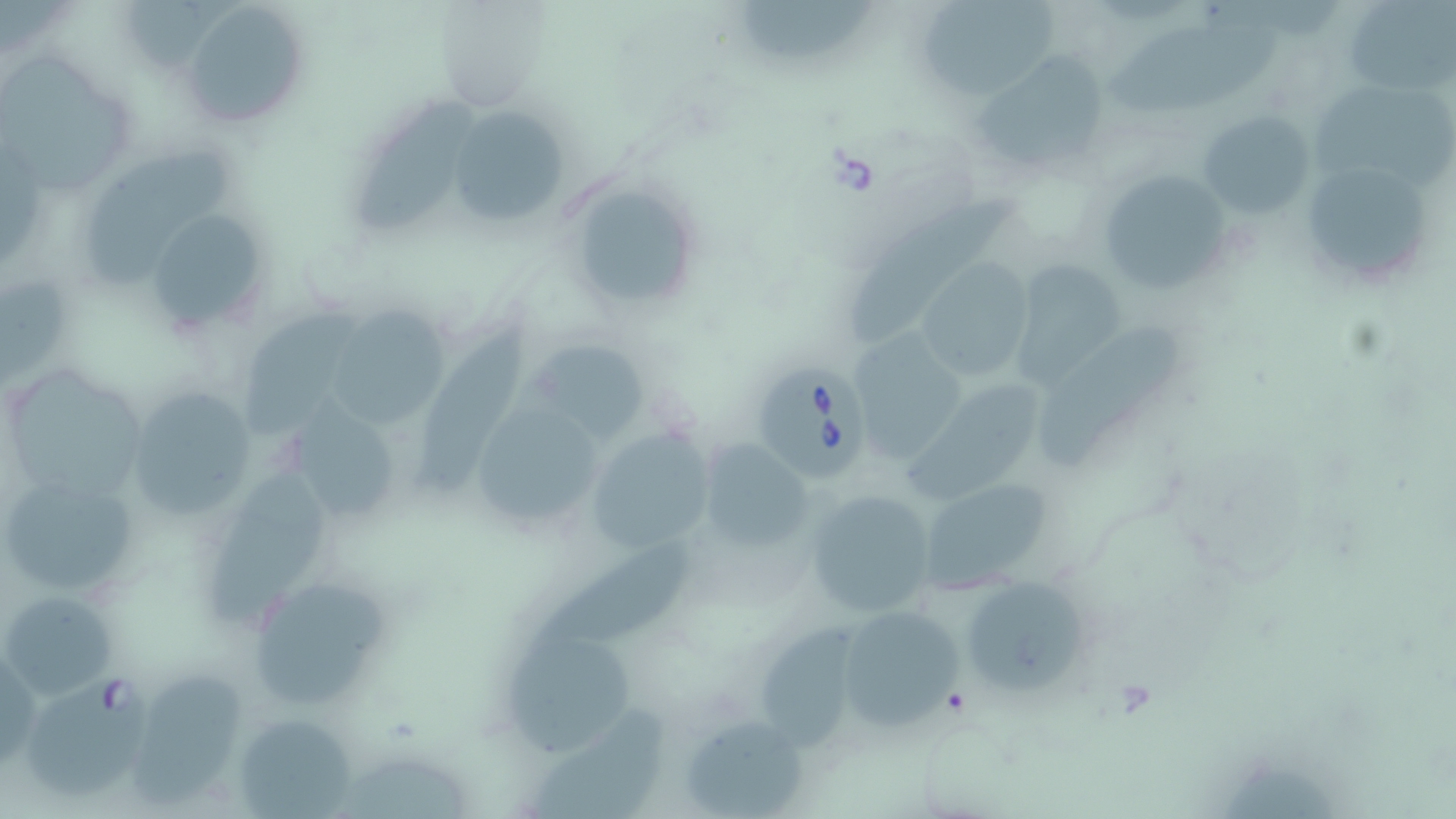
Summary:
  - Coordinate format: approximate bounding boxes as named x1/y1/x2/y2 corners in pixels
  - Uninfected red blood cell locations: (x1=730, y1=0, x2=879, y2=61), (x1=919, y1=0, x2=1058, y2=101), (x1=1343, y1=0, x2=1454, y2=94), (x1=183, y1=1, x2=310, y2=127), (x1=433, y1=3, x2=547, y2=113), (x1=1110, y1=19, x2=1282, y2=110), (x1=975, y1=52, x2=1114, y2=173), (x1=4, y1=54, x2=136, y2=192), (x1=1315, y1=86, x2=1456, y2=188), (x1=354, y1=100, x2=477, y2=240), (x1=445, y1=105, x2=565, y2=227), (x1=1198, y1=109, x2=1316, y2=221), (x1=86, y1=143, x2=225, y2=289), (x1=1299, y1=157, x2=1439, y2=287), (x1=1094, y1=168, x2=1235, y2=296), (x1=566, y1=172, x2=703, y2=312), (x1=847, y1=200, x2=1013, y2=350), (x1=142, y1=207, x2=276, y2=338), (x1=913, y1=258, x2=1032, y2=383), (x1=1007, y1=258, x2=1130, y2=386), (x1=333, y1=301, x2=448, y2=425), (x1=248, y1=307, x2=360, y2=440), (x1=1045, y1=323, x2=1180, y2=464), (x1=416, y1=324, x2=529, y2=499), (x1=855, y1=327, x2=971, y2=467), (x1=527, y1=337, x2=653, y2=442), (x1=3, y1=364, x2=152, y2=507), (x1=914, y1=379, x2=1039, y2=498), (x1=126, y1=385, x2=259, y2=519), (x1=463, y1=395, x2=611, y2=540), (x1=276, y1=403, x2=408, y2=524), (x1=583, y1=429, x2=713, y2=553), (x1=695, y1=440, x2=813, y2=554), (x1=0, y1=472, x2=140, y2=600), (x1=917, y1=476, x2=1061, y2=589), (x1=203, y1=477, x2=328, y2=625), (x1=802, y1=488, x2=938, y2=621), (x1=542, y1=539, x2=697, y2=638), (x1=960, y1=575, x2=1091, y2=695), (x1=254, y1=586, x2=389, y2=703), (x1=3, y1=591, x2=119, y2=699), (x1=835, y1=604, x2=966, y2=738), (x1=760, y1=619, x2=847, y2=749), (x1=508, y1=628, x2=635, y2=764), (x1=132, y1=672, x2=253, y2=810), (x1=530, y1=701, x2=671, y2=819), (x1=232, y1=710, x2=361, y2=818), (x1=679, y1=714, x2=811, y2=816), (x1=345, y1=757, x2=475, y2=819)
  - Babesia divergens-infected red blood cell locations: (x1=745, y1=358, x2=878, y2=485), (x1=33, y1=670, x2=153, y2=801)
  - Slide-level diagnosis: Babesia divergens
  - Field of view: single
  - Image size: 1456×819 pixels
  - Modality: light microscopy
  - Magnification: 1000x
  - Preparation: thin blood smear
  - Stain: May-Grünwald-Giemsa